Report the malaria status of this cell.
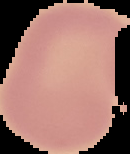

Uninfected.

Summary:
  - Image size: 130×154 pixels
  - Preparation: thin blood smear
  - Image type: segmented cell region with the area outside set to black